State which parasite is depicted.
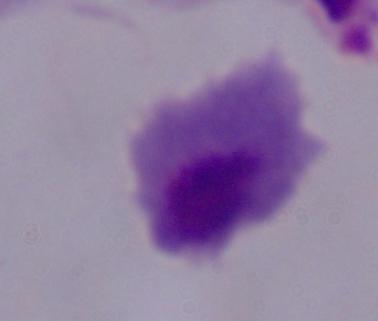

A trichomonad.

Summary:
  - Modality: photomicrograph
  - Magnification: 1000x